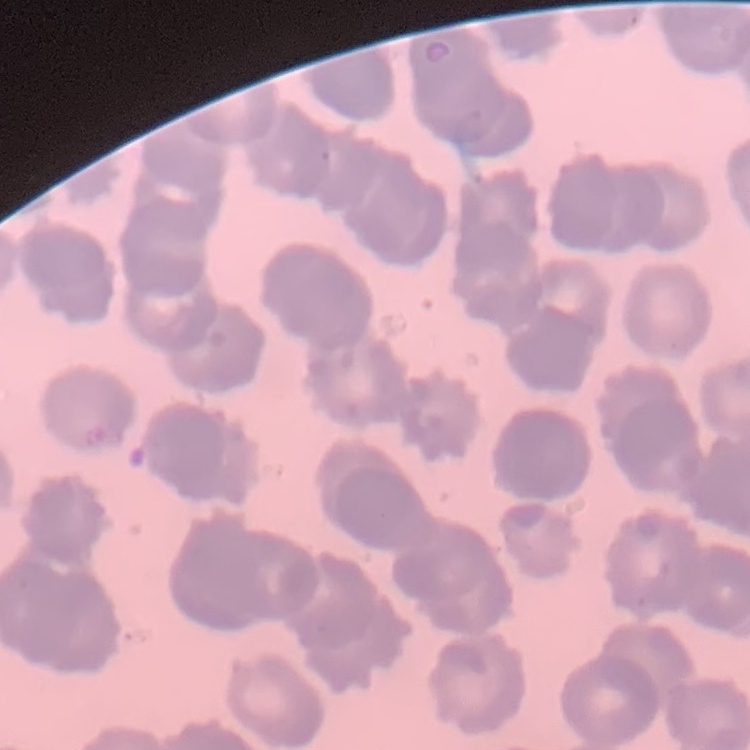

red_blood_cell_morphology: rouleaux formation
image_type: square crop of a larger photomicrograph
preparation: thin blood film
stain: Field's or Giemsa